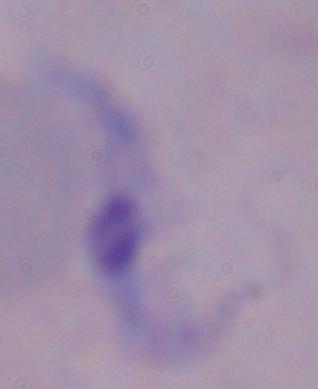

Captured at 1000x magnification. Photomicrograph. A trypanosome is seen.